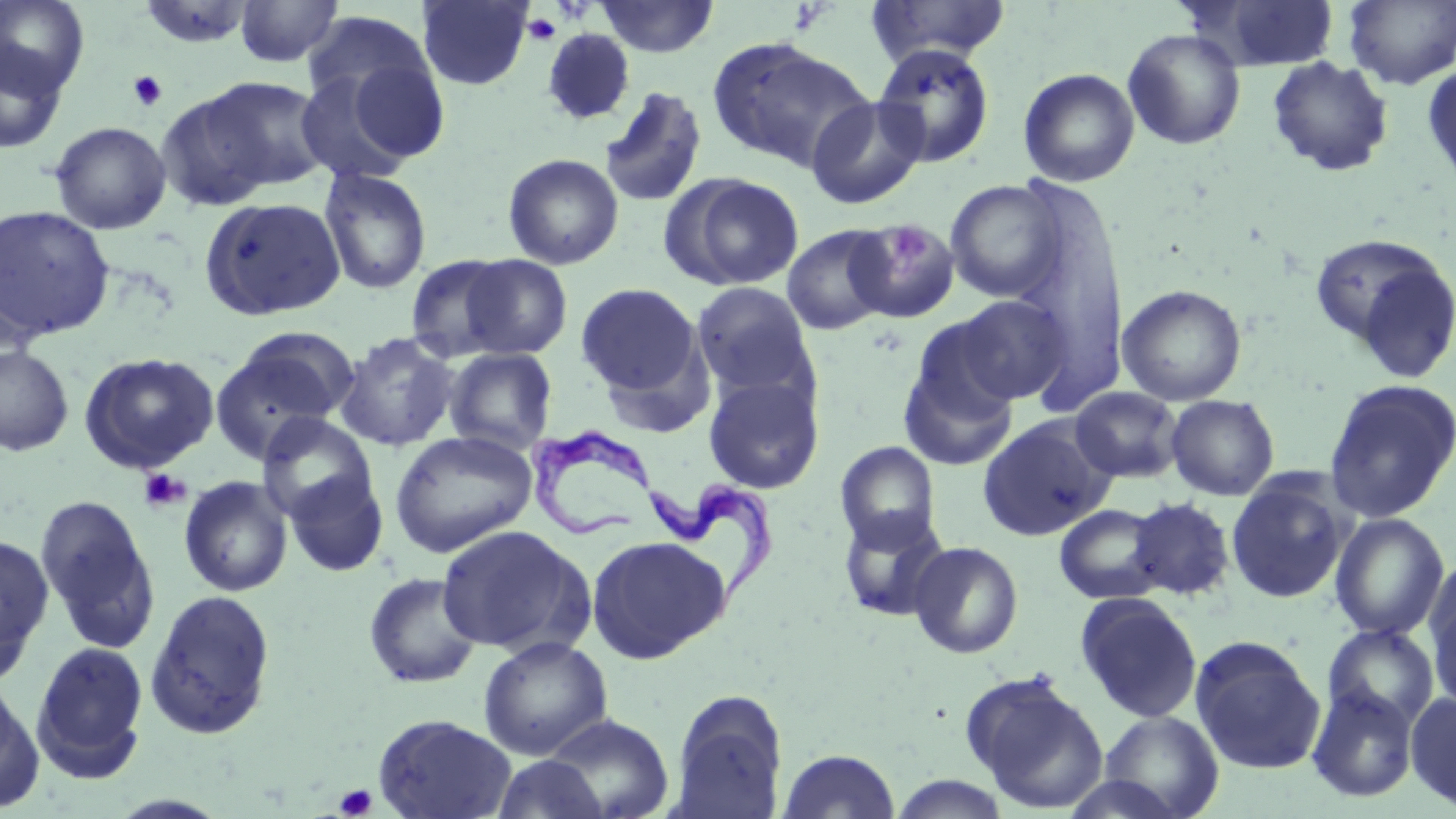

Summary:
  - Coordinate format: approximate bounding boxes as (x1, y1, x2, y2) in pixels
  - Trypanosoma brucei locations: (527, 426, 663, 544), (649, 479, 784, 618)
  - Uninfected red blood cell locations: (0, 0, 91, 98), (234, 0, 344, 68), (416, 0, 533, 90), (594, 0, 719, 57), (1197, 0, 1342, 71), (1344, 0, 1456, 90), (137, 1, 257, 49), (865, 1, 1012, 66), (301, 11, 438, 115), (1122, 27, 1246, 151), (542, 28, 635, 126), (706, 36, 872, 174), (0, 41, 68, 154), (873, 43, 996, 168), (333, 51, 453, 165), (1267, 56, 1395, 177), (1422, 61, 1456, 198), (293, 67, 424, 185), (1018, 67, 1140, 187), (175, 76, 328, 201), (598, 86, 708, 208), (805, 95, 929, 209), (49, 121, 172, 235), (503, 153, 624, 270), (318, 167, 432, 295), (666, 174, 806, 290), (1009, 178, 1128, 406), (945, 179, 1066, 303), (199, 196, 347, 321), (0, 205, 115, 344), (847, 219, 960, 322), (782, 225, 895, 336), (1313, 238, 1456, 382), (404, 254, 517, 361), (457, 254, 573, 360), (692, 282, 817, 399), (576, 283, 704, 403), (1117, 284, 1247, 406), (952, 294, 1072, 404), (898, 328, 1023, 473), (335, 332, 460, 452), (209, 336, 351, 463), (0, 345, 74, 456), (444, 347, 558, 454), (78, 351, 220, 473), (703, 373, 825, 494), (1323, 379, 1456, 524), (1070, 386, 1184, 482), (1165, 394, 1280, 500), (257, 413, 377, 526), (978, 416, 1112, 540), (389, 430, 538, 558), (836, 441, 941, 551), (283, 468, 388, 578), (1225, 474, 1350, 603), (179, 476, 293, 597), (35, 495, 159, 652), (1126, 497, 1236, 601), (1054, 503, 1167, 604), (837, 507, 951, 622), (1329, 513, 1451, 640), (435, 524, 593, 657), (0, 534, 54, 679), (586, 534, 732, 663), (908, 541, 1024, 659), (1426, 566, 1456, 705), (363, 572, 483, 689), (145, 588, 276, 740), (1075, 593, 1203, 723), (1322, 623, 1439, 730), (477, 636, 613, 760), (1190, 637, 1326, 775), (32, 641, 148, 780), (960, 670, 1109, 814), (0, 678, 44, 812), (1306, 683, 1420, 803), (670, 689, 788, 817), (1406, 692, 1456, 811), (1097, 710, 1224, 818), (372, 714, 518, 819), (542, 714, 674, 817), (777, 748, 902, 818), (491, 754, 609, 818), (1059, 773, 1190, 819)
  - Platelet locations: (523, 13, 561, 46), (127, 70, 167, 112), (137, 467, 192, 514), (334, 784, 377, 818)
  - Slide-level diagnosis: Trypanosoma brucei
  - Modality: optical microscopy
  - Preparation: thin blood smear
  - Image size: 1456×819 pixels
  - Stain: May-Grünwald-Giemsa
  - Magnification: 1000x
  - Field of view: single